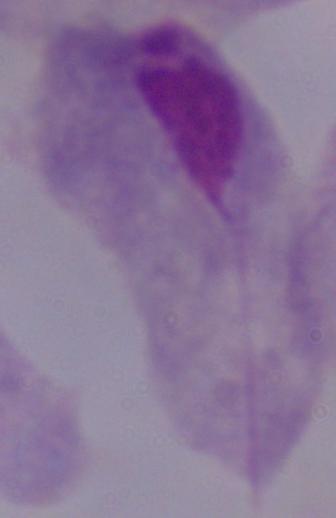 Captured at 1000x magnification. Photomicrograph. A trichomonad is shown.